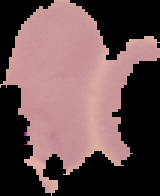

image_type: cell region segmented out of the field of view; surrounding area masked to black
preparation: thin blood smear
malaria_status: parasitized
image_size: 160×196 pixels